Report the malaria status of this cell.
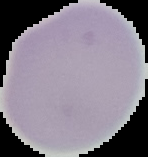
Uninfected.

Image is 148×157 pixels. The area outside the segmented cell region is set to black. From a thin blood smear.